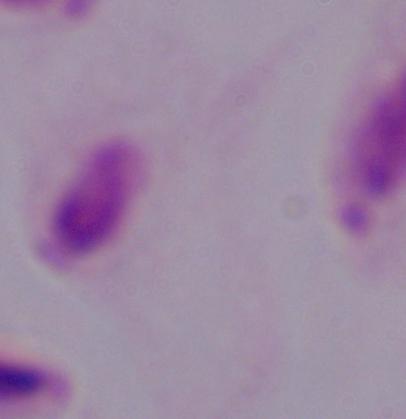
Micrograph. Captured at 1000x magnification. A trichomonad is seen.